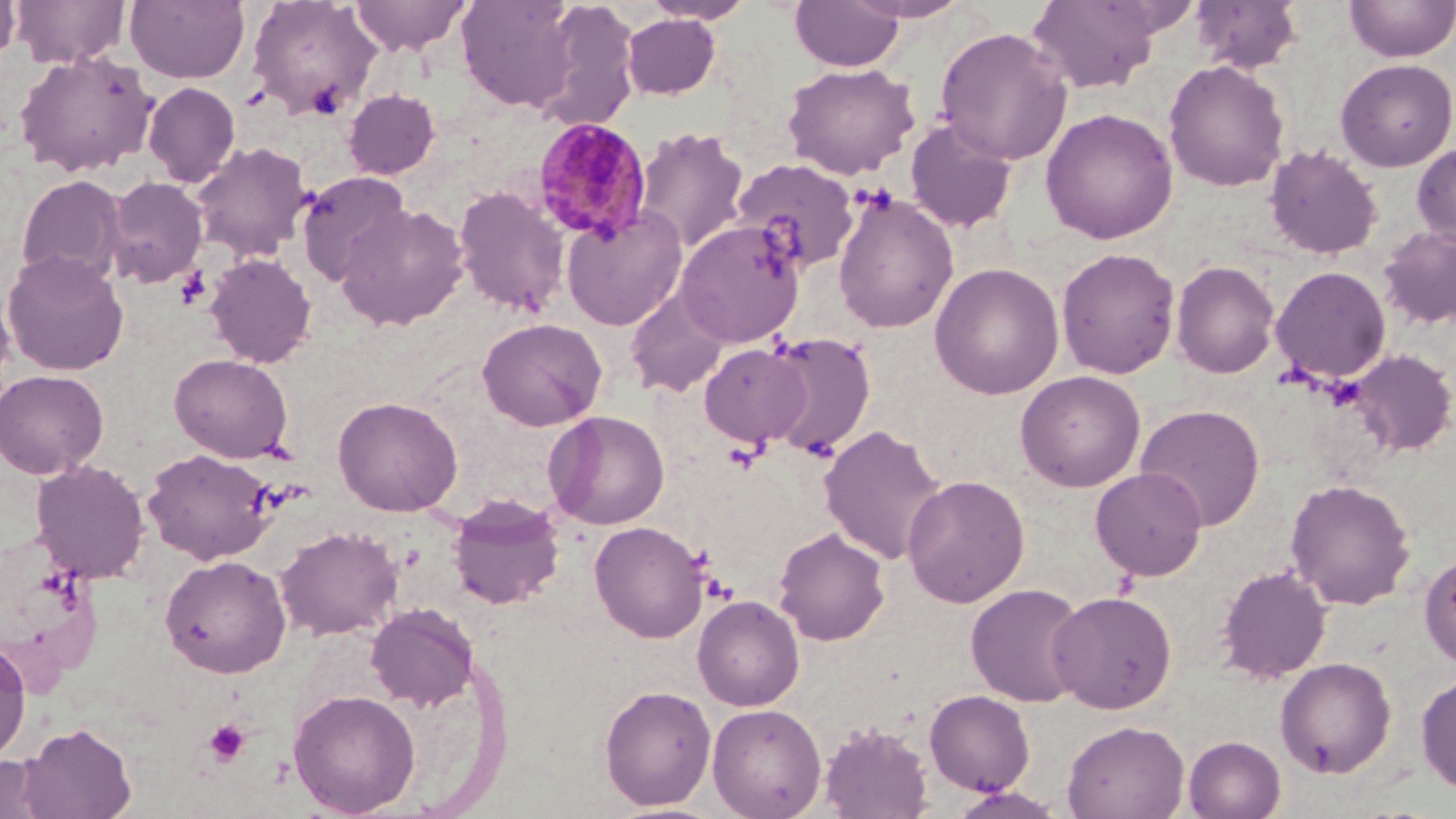

slide-level diagnosis = Plasmodium malariae
preparation = thin blood film
uninfected red blood cell locations = approximate bounding boxes as [x1, y1, x2, y2] in pixels: [0, 0, 20, 66], [12, 0, 130, 69], [125, 0, 250, 83], [247, 0, 380, 120], [350, 0, 472, 55], [454, 0, 583, 113], [790, 0, 905, 71], [844, 0, 973, 23], [1190, 0, 1303, 74], [1344, 0, 1456, 62], [640, 1, 757, 25], [1027, 1, 1166, 93], [531, 2, 642, 130], [621, 13, 721, 99], [935, 26, 1073, 165], [14, 50, 159, 178], [1335, 58, 1456, 171], [1163, 59, 1290, 192], [781, 62, 920, 180], [143, 82, 240, 187], [342, 88, 441, 179], [1040, 107, 1178, 244], [905, 117, 1018, 234], [632, 127, 749, 255], [190, 141, 313, 262], [1412, 142, 1456, 247], [1264, 145, 1383, 259], [731, 158, 860, 273], [296, 171, 411, 287], [15, 174, 127, 287], [103, 176, 208, 288], [453, 186, 571, 317], [832, 187, 959, 334], [335, 203, 470, 330], [561, 207, 688, 331], [675, 219, 806, 348], [1377, 226, 1456, 330], [1056, 247, 1180, 379], [2, 250, 129, 376], [204, 252, 317, 368], [1170, 260, 1280, 379], [929, 262, 1065, 400], [1270, 265, 1392, 383], [0, 286, 15, 390], [625, 287, 731, 397], [477, 318, 607, 431], [762, 330, 877, 460], [700, 343, 811, 449], [1348, 348, 1456, 456], [169, 353, 293, 463], [0, 369, 109, 479], [1015, 370, 1147, 492], [332, 396, 463, 516], [1134, 403, 1266, 531], [544, 410, 670, 530], [819, 424, 948, 566], [143, 447, 279, 565], [30, 459, 150, 583], [1090, 466, 1208, 581], [902, 474, 1030, 607], [1284, 478, 1416, 609], [448, 494, 565, 609], [590, 520, 710, 643], [274, 525, 403, 641], [773, 526, 890, 646], [1418, 551, 1456, 671], [159, 554, 292, 677], [1216, 565, 1333, 684], [966, 583, 1089, 707], [1047, 590, 1177, 713], [692, 594, 805, 711], [365, 602, 480, 711], [0, 637, 31, 766], [1275, 656, 1397, 778], [1416, 672, 1456, 795], [599, 684, 717, 810], [288, 687, 421, 817], [924, 689, 1035, 795], [707, 702, 827, 819], [1062, 720, 1189, 819], [20, 721, 137, 818], [819, 722, 934, 819], [1184, 735, 1286, 819], [0, 753, 58, 819], [946, 787, 1068, 819]
magnification = 1000x
modality = optical microscopy
stain = May-Grünwald-Giemsa
field of view = single
Plasmodium malariae-infected red blood cell locations = approximate bounding boxes as [x1, y1, x2, y2] in pixels: [531, 117, 653, 246]
platelet locations = approximate bounding boxes as [x1, y1, x2, y2] in pixels: [175, 267, 212, 310], [724, 441, 766, 473], [204, 718, 251, 766]
image size = 1456×819 pixels